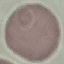 Malaria status: uninfected. Thin smear of blood. Acquired by smartphone through the microscope eyepiece. Automatically extracted cell patch, resized to 64 × 64 pixels. Giemsa stain.